Which red blood cells are Plasmodium falciparum-infected, and which are of indeterminate infection status?
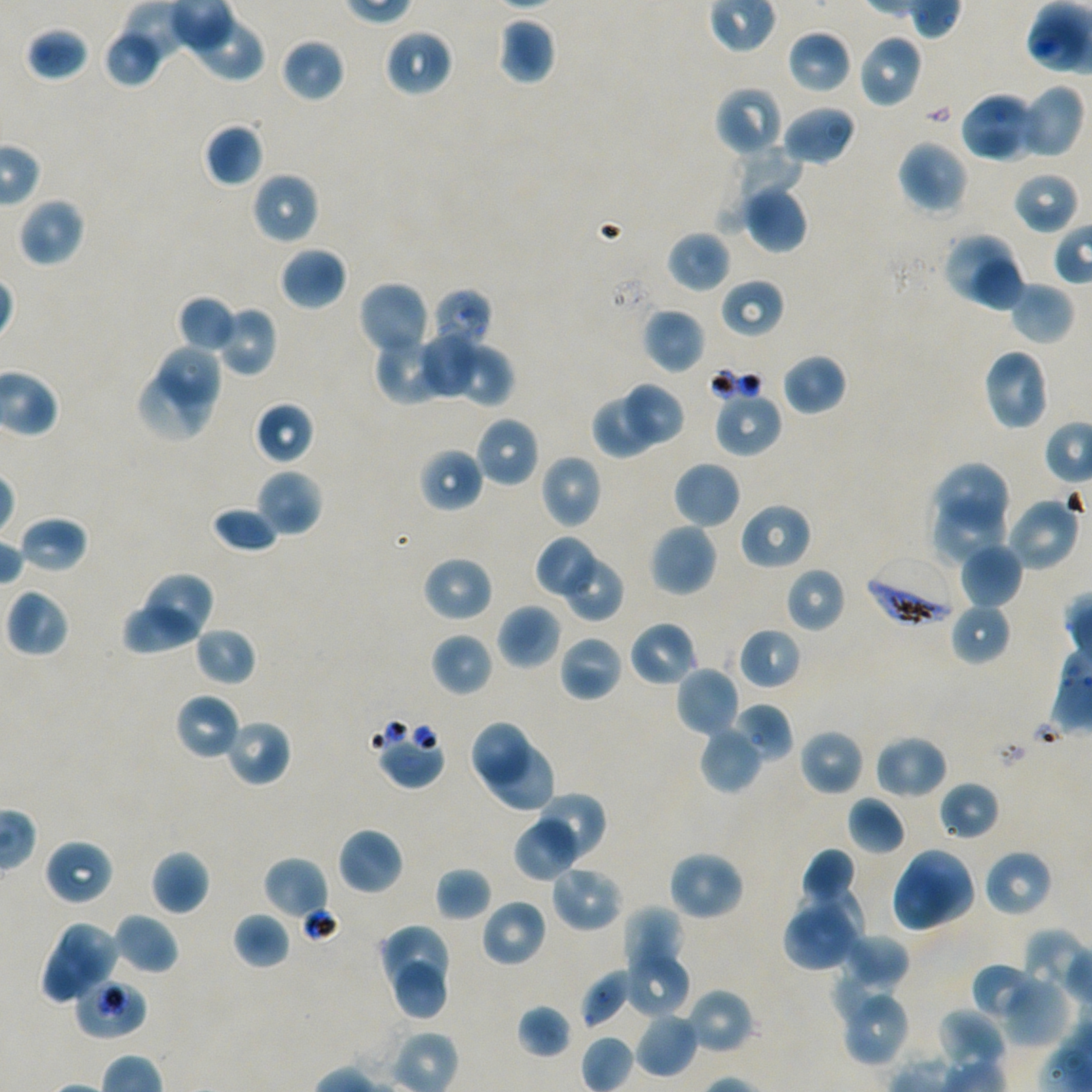

Approximate bounding boxes as {x1, y1, x2, y2} in pixels. Not every red blood cell is marked.
Infected red blood cells: {864, 556, 958, 629}.
Red blood cells of indeterminate infection status: {377, 730, 445, 789}, {73, 977, 147, 1040}.

Locations of uninfected red blood cells: {185, 11, 267, 81}, {497, 17, 557, 86}, {25, 25, 90, 82}, {103, 28, 163, 88}, {382, 28, 452, 97}, {787, 29, 852, 95}, {856, 34, 923, 109}, {280, 37, 346, 103}, {1015, 84, 1084, 160}, {714, 86, 784, 158}, {962, 91, 1039, 164}, {782, 104, 857, 166}, {203, 123, 264, 187}, {896, 139, 969, 214}, {710, 147, 803, 238}, {1012, 170, 1080, 234}, {251, 172, 320, 245}, {742, 181, 809, 253}, {18, 197, 86, 268}, {666, 230, 730, 293}, {941, 231, 1014, 304}, {280, 246, 347, 310}, {974, 259, 1023, 314}, {720, 278, 785, 338}, {358, 280, 431, 358}, {1008, 282, 1075, 345}, {429, 289, 493, 356}, {177, 295, 237, 354}, {214, 305, 277, 377}, {642, 307, 705, 374}, {421, 322, 479, 397}, {372, 331, 443, 403}, {452, 337, 513, 408}, {160, 346, 223, 407}, {982, 347, 1051, 432}, {782, 353, 847, 416}, {136, 369, 215, 444}, {622, 383, 685, 445}, {591, 389, 668, 459}, {713, 391, 782, 458}, {255, 401, 314, 465}, {474, 415, 540, 488}, {418, 448, 484, 512}, {539, 454, 602, 529}, {674, 460, 742, 529}, {933, 460, 1011, 537}, {255, 469, 323, 537}, {931, 492, 1008, 564}, {1005, 494, 1080, 572}, {739, 502, 812, 570}, {211, 505, 280, 555}, {18, 515, 89, 574}, {648, 522, 718, 598}, {537, 538, 596, 596}, {960, 541, 1022, 608}, {422, 556, 493, 623}, {566, 558, 623, 620}, {785, 567, 847, 633}, {136, 571, 215, 645}, {5, 588, 70, 657}, {497, 603, 562, 670}, {950, 603, 1011, 665}, {122, 606, 206, 657}, {630, 621, 699, 688}, {194, 625, 257, 686}, {738, 627, 802, 690}, {431, 632, 493, 697}, {558, 634, 623, 703}, {676, 665, 739, 738}, {175, 693, 242, 761}, {730, 703, 793, 762}, {224, 718, 291, 786}, {471, 722, 534, 789}, {699, 725, 764, 794}, {798, 729, 864, 796}, {874, 733, 947, 799}, {481, 739, 558, 813}, {938, 781, 1001, 841}, {536, 790, 607, 858}, {847, 797, 905, 856}, {513, 815, 582, 881}, {337, 827, 403, 896}, {44, 839, 114, 905}, {801, 848, 856, 909}, {907, 848, 975, 922}, {982, 848, 1053, 917}, {151, 850, 210, 915}, {666, 850, 745, 922}, {263, 856, 329, 922}, {549, 864, 624, 933}, {434, 867, 493, 922}, {891, 867, 959, 933}, {795, 888, 867, 956}, {481, 898, 547, 968}, {621, 905, 684, 979}, {783, 909, 855, 971}, {232, 912, 291, 969}, {112, 913, 179, 976}, {58, 920, 120, 982}, {380, 923, 453, 991}, {841, 932, 910, 994}, {41, 941, 103, 1004}, {624, 947, 690, 1017}, {393, 962, 447, 1019}, {831, 964, 898, 1023}, {974, 964, 1037, 1023}, {579, 970, 632, 1029}, {996, 983, 1068, 1049}, {837, 986, 910, 1067}, {685, 987, 754, 1055}, {517, 1004, 573, 1059}, {938, 1008, 1008, 1073}, {634, 1012, 699, 1078}, {579, 1035, 635, 1092}. Thin blood smear. One field from this slide. 100x objective under oil immersion, numerical aperture 1.45. Giemsa-stained preparation. Donor blood group A+/O+. Image is 1092×1092 pixels. Plasmodium falciparum strain NF54 maintained in static in-vitro culture.